Assess this cell for malaria.
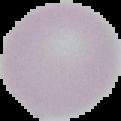
It is uninfected.

Summary:
  - Preparation: thin blood smear
  - Image size: 121×121 pixels
  - Image type: cell region segmented out of the field of view; surrounding area masked to black